Locate and identify every blood parasite.
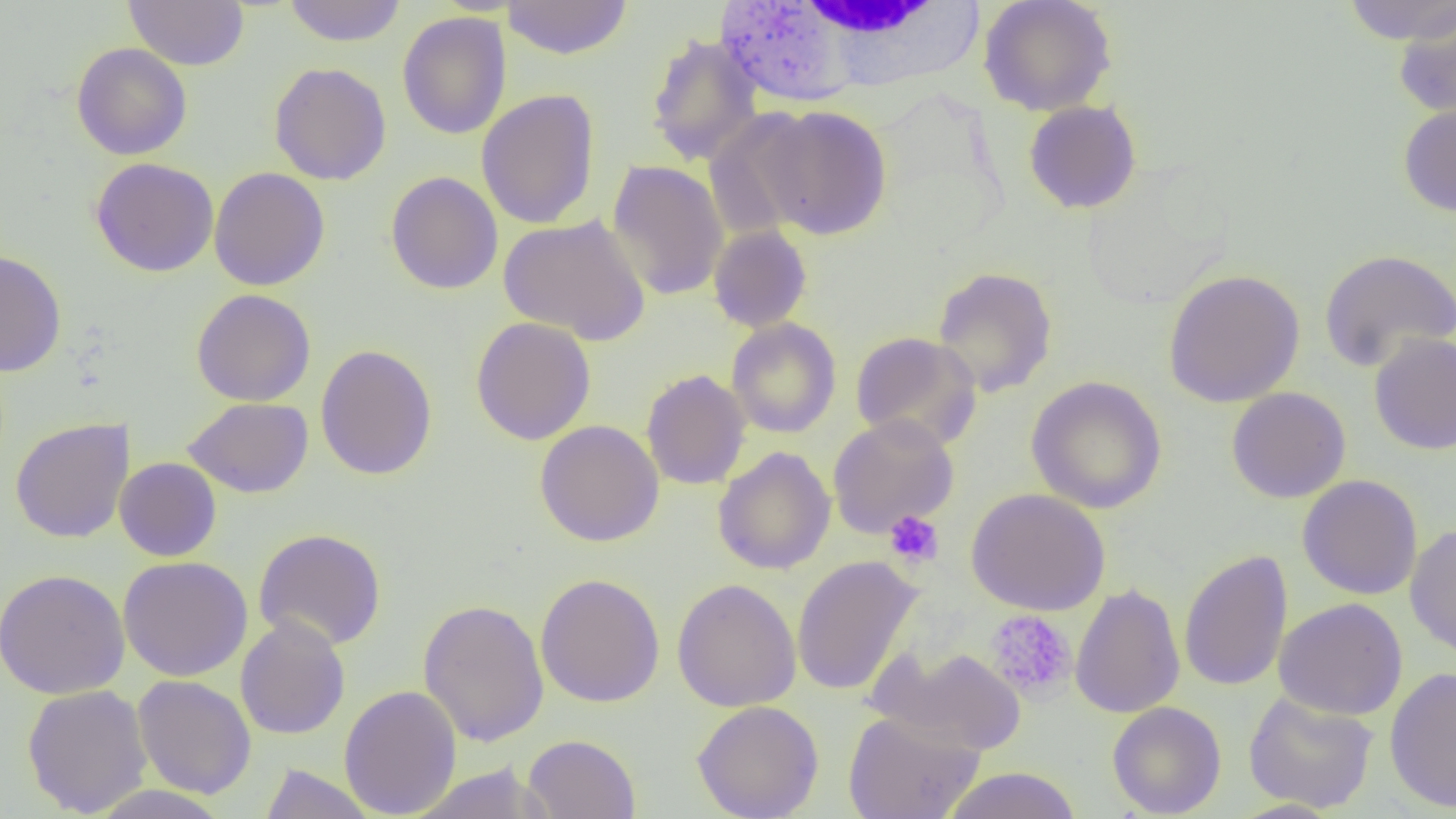

No blood parasites seen.

Approximate bounding boxes as (x1,y1)-(x2,y2) corner pairs in pixels. Uninfected red blood cell locations: (123,0)-(249,70), (283,0)-(407,46), (502,0)-(633,60), (979,0)-(1117,116), (1340,0)-(1456,44), (1392,7)-(1456,120), (397,12)-(511,140), (645,33)-(764,168), (71,43)-(192,160), (269,62)-(392,185), (476,89)-(600,229), (1023,100)-(1142,214), (1398,103)-(1456,218), (759,105)-(893,240), (702,109)-(820,240), (90,158)-(219,277), (607,159)-(729,302), (209,167)-(330,291), (386,171)-(503,295), (499,214)-(651,345), (708,225)-(813,332), (0,248)-(67,377), (1318,249)-(1456,373), (931,266)-(1059,398), (1162,268)-(1306,408), (191,288)-(316,406), (470,317)-(597,445), (726,318)-(841,439), (850,331)-(982,451), (1369,332)-(1456,456), (315,344)-(438,481), (641,369)-(751,490), (1026,376)-(1167,514), (1226,387)-(1351,503), (183,397)-(314,498), (827,415)-(959,538), (10,418)-(134,543), (535,419)-(664,546), (712,446)-(836,575), (115,457)-(222,562), (1297,475)-(1423,600), (966,488)-(1110,615), (1404,523)-(1456,659), (253,528)-(387,651), (1178,549)-(1293,692), (117,556)-(253,681), (791,556)-(923,696), (0,568)-(130,699), (535,573)-(665,708), (672,578)-(801,712), (1069,583)-(1186,719), (1273,597)-(1409,720), (418,598)-(550,748), (235,616)-(350,740), (871,645)-(1028,756), (1385,666)-(1456,813), (133,675)-(257,799), (21,684)-(153,817), (339,684)-(462,818), (1243,691)-(1379,813), (692,700)-(824,819), (1107,701)-(1226,818), (843,710)-(986,819), (523,733)-(641,819), (410,762)-(555,819), (258,763)-(378,819), (940,767)-(1082,819), (84,785)-(234,819), (1227,798)-(1345,819). White blood cell locations: (784,0)-(985,84). Platelet locations: (884,509)-(944,568), (984,610)-(1078,702). Slide-level diagnosis: no evidence of blood parasites. Thin blood film. Optical microscopy. Captured at 1000x magnification. One field of a larger specimen. Image is 1456×819 pixels.